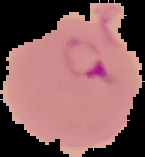
Image is 145×157 pixels. From a thin blood film. Malaria status: parasitized. Segmented cell region on a black background.